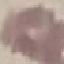

malaria status = uninfected
image type = cell patch, automatically extracted from a larger field of view and resized to 64 × 64 pixels
preparation = thin blood film
stain = Giemsa
capture = smartphone camera at the microscope eyepiece